Point out each leukocyte.
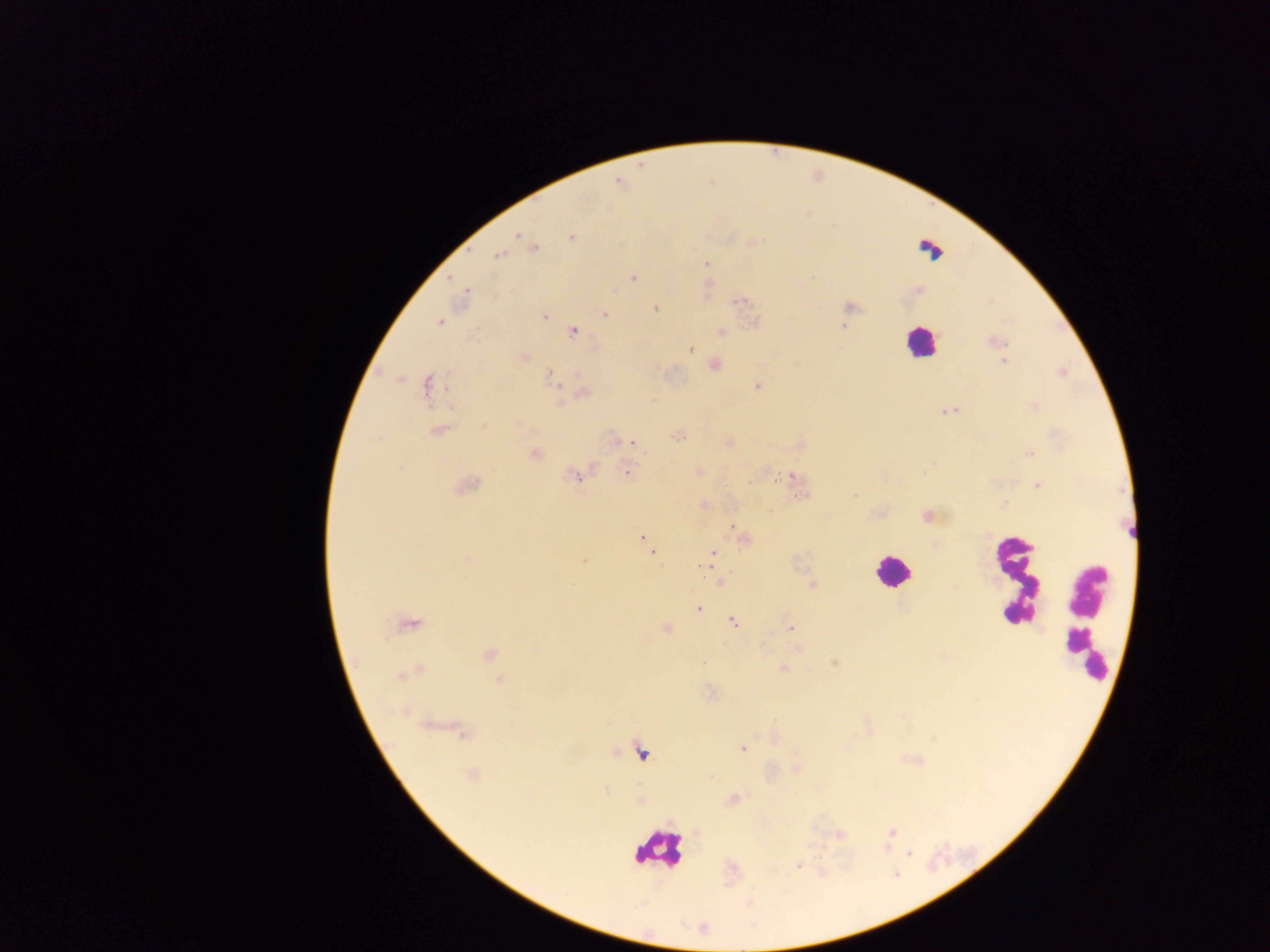
Approximate centers as [x, y] in pixels.
Leukocytes (some below the resolvable threshold): [929, 245], [919, 342], [891, 571], [1013, 579], [1084, 619], [659, 850].

Malaria parasite locations: [517, 235], [571, 237], [534, 248], [498, 255], [706, 263], [633, 279], [466, 292], [739, 301], [850, 307], [655, 308], [604, 315], [544, 316], [439, 321], [842, 326], [573, 331], [994, 341], [691, 349], [524, 357], [1005, 362], [715, 365], [550, 376], [427, 386], [757, 386], [585, 394], [560, 403], [949, 411], [439, 431], [677, 436], [379, 439], [632, 443], [534, 453], [1028, 453], [627, 473], [577, 476], [791, 477], [1038, 485], [466, 487], [854, 496], [927, 516], [733, 526], [643, 539], [651, 552], [713, 552], [702, 566], [812, 585], [698, 609], [733, 621], [409, 626], [791, 627], [667, 628], [798, 649], [489, 655], [704, 663], [783, 669], [410, 673], [500, 681], [462, 730], [742, 749], [472, 775], [891, 832], [841, 834], [909, 854], [798, 866]. Image is 1270×952 pixels. Sample from Ghana. Mobile-phone photograph taken through the microscope. Thick blood film. One field of view.